Name the parasite shown.
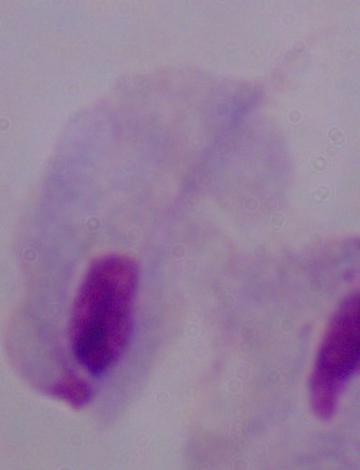
A trichomonad.

Summary:
  - Modality: photomicrograph
  - Magnification: 1000x